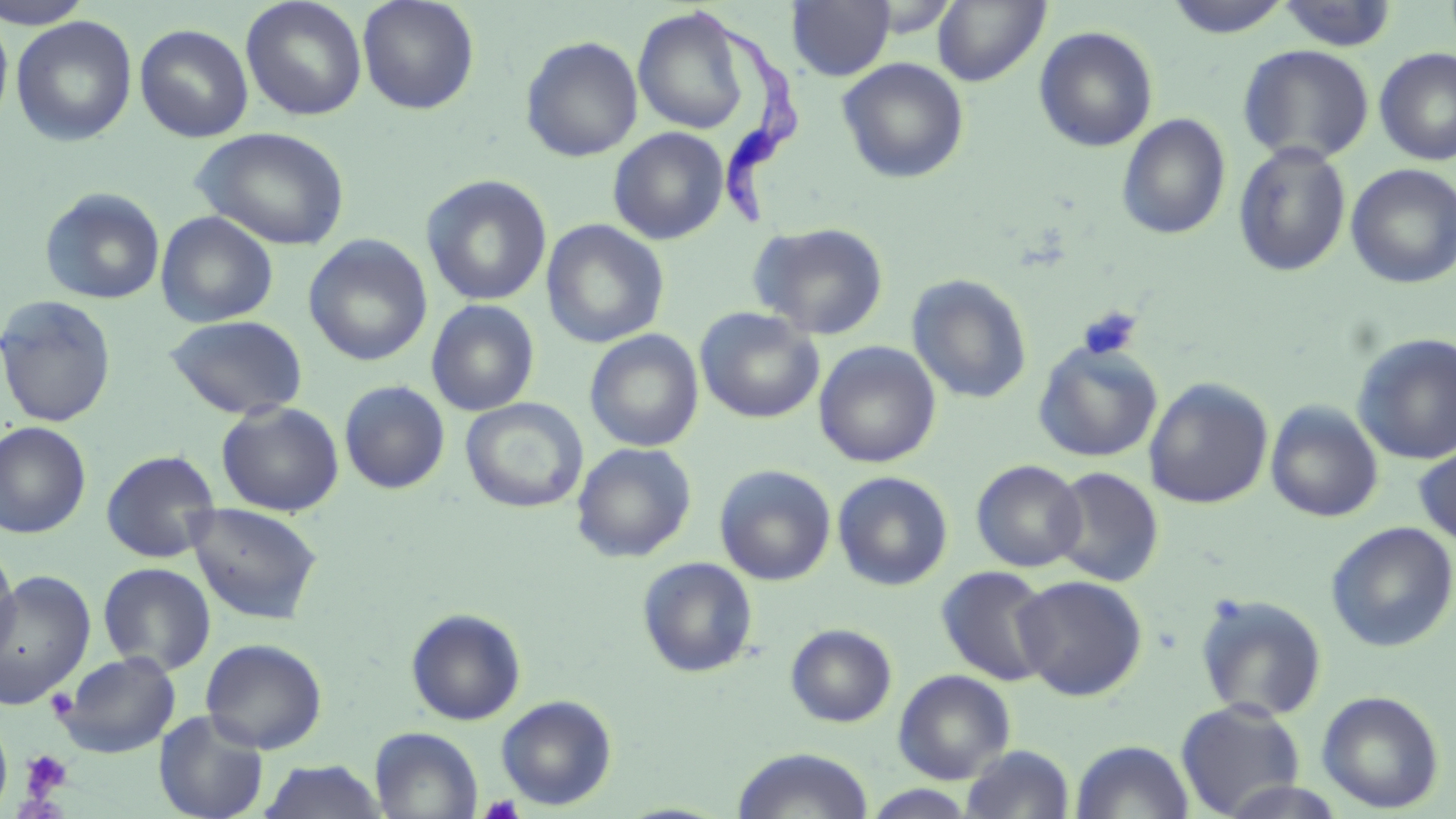
slide-level diagnosis = Trypanosoma brucei
modality = light microscopy
preparation = thin blood film
Trypanosoma brucei locations = approximate bounding boxes as (x1, y1, x2, y2) in pixels: (686, 2, 809, 235)
magnification = 1000x
platelet locations = approximate bounding boxes as (x1, y1, x2, y2) in pixels: (1077, 306, 1143, 361), (46, 688, 77, 720), (20, 749, 73, 800), (478, 794, 525, 818)
field of view = one of a larger specimen
image size = 1456×819 pixels
uninfected red blood cell locations = approximate bounding boxes as (x1, y1, x2, y2) in pixels: (0, 0, 95, 28), (241, 0, 368, 121), (357, 0, 480, 115), (1162, 0, 1295, 39), (786, 1, 896, 82), (933, 1, 1050, 87), (1275, 1, 1399, 52), (633, 7, 753, 136), (0, 10, 14, 135), (11, 15, 138, 146), (135, 24, 254, 142), (1033, 25, 1159, 153), (519, 35, 644, 163), (1237, 44, 1375, 164), (1374, 47, 1456, 166), (837, 57, 970, 184), (1116, 112, 1231, 241), (191, 126, 352, 251), (608, 127, 729, 245), (1233, 141, 1352, 277), (1345, 164, 1456, 289), (421, 174, 553, 307), (40, 187, 166, 305), (155, 211, 278, 328), (541, 219, 669, 348), (749, 222, 889, 341), (304, 235, 432, 367), (907, 274, 1033, 404), (0, 295, 118, 428), (425, 299, 540, 416), (695, 307, 824, 424), (164, 314, 308, 420), (585, 329, 704, 452), (1352, 332, 1456, 465), (813, 341, 941, 468), (1033, 342, 1163, 462), (1144, 378, 1273, 509), (338, 380, 450, 494), (460, 398, 588, 514), (1266, 400, 1383, 523), (216, 401, 344, 517), (0, 422, 92, 539), (1414, 438, 1456, 550), (571, 442, 697, 563), (100, 449, 221, 563), (972, 459, 1086, 573), (715, 464, 836, 586), (1049, 466, 1164, 587), (832, 471, 954, 591), (186, 501, 324, 625), (1326, 522, 1456, 652), (0, 545, 19, 667), (637, 556, 759, 678), (98, 562, 216, 676), (936, 565, 1055, 686), (0, 570, 96, 708), (1013, 574, 1148, 701), (1194, 593, 1328, 722), (406, 608, 527, 725), (785, 623, 897, 728), (200, 637, 327, 754), (55, 650, 181, 758), (893, 669, 1016, 784), (1316, 690, 1445, 814), (496, 695, 617, 811), (1175, 699, 1306, 817), (153, 710, 269, 819), (0, 718, 12, 813), (370, 727, 483, 818), (1070, 740, 1194, 819), (960, 744, 1076, 818), (731, 747, 874, 819), (260, 759, 386, 819), (862, 785, 980, 818)
stain = May-Grünwald-Giemsa